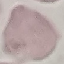

Malaria status: uninfected. Cell patch, automatically extracted from a larger field of view and resized to 64 × 64 pixels. Thin blood smear. Giemsa-stained preparation. Acquired by smartphone through the microscope eyepiece.